Assess the morphology of the red blood cells.
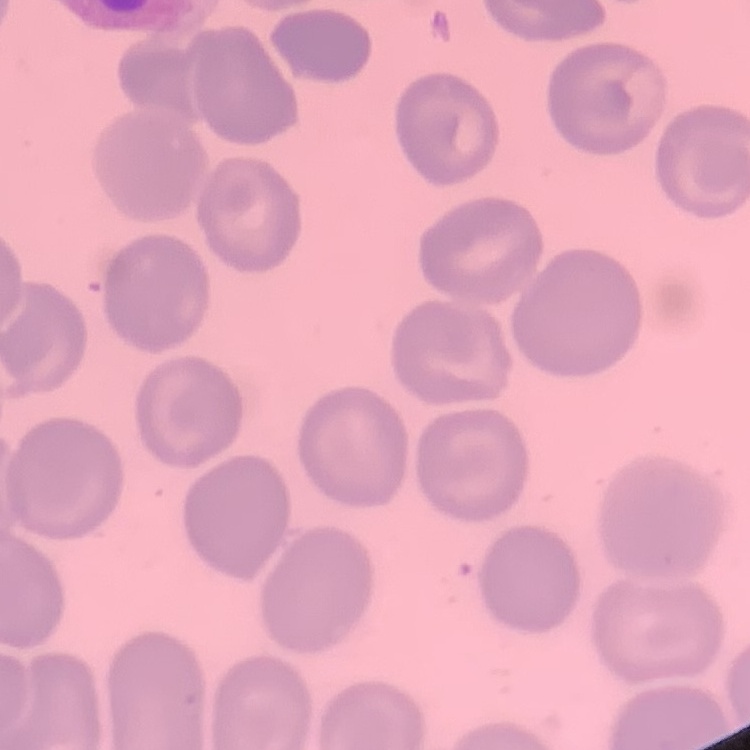

They show no rouleaux formation.

{
  "stain": "Field's or Giemsa",
  "preparation": "thin blood smear",
  "image_type": "one tile cut from a larger photomicrograph"
}